Give the position of every malaria parasite and every leukocyte.
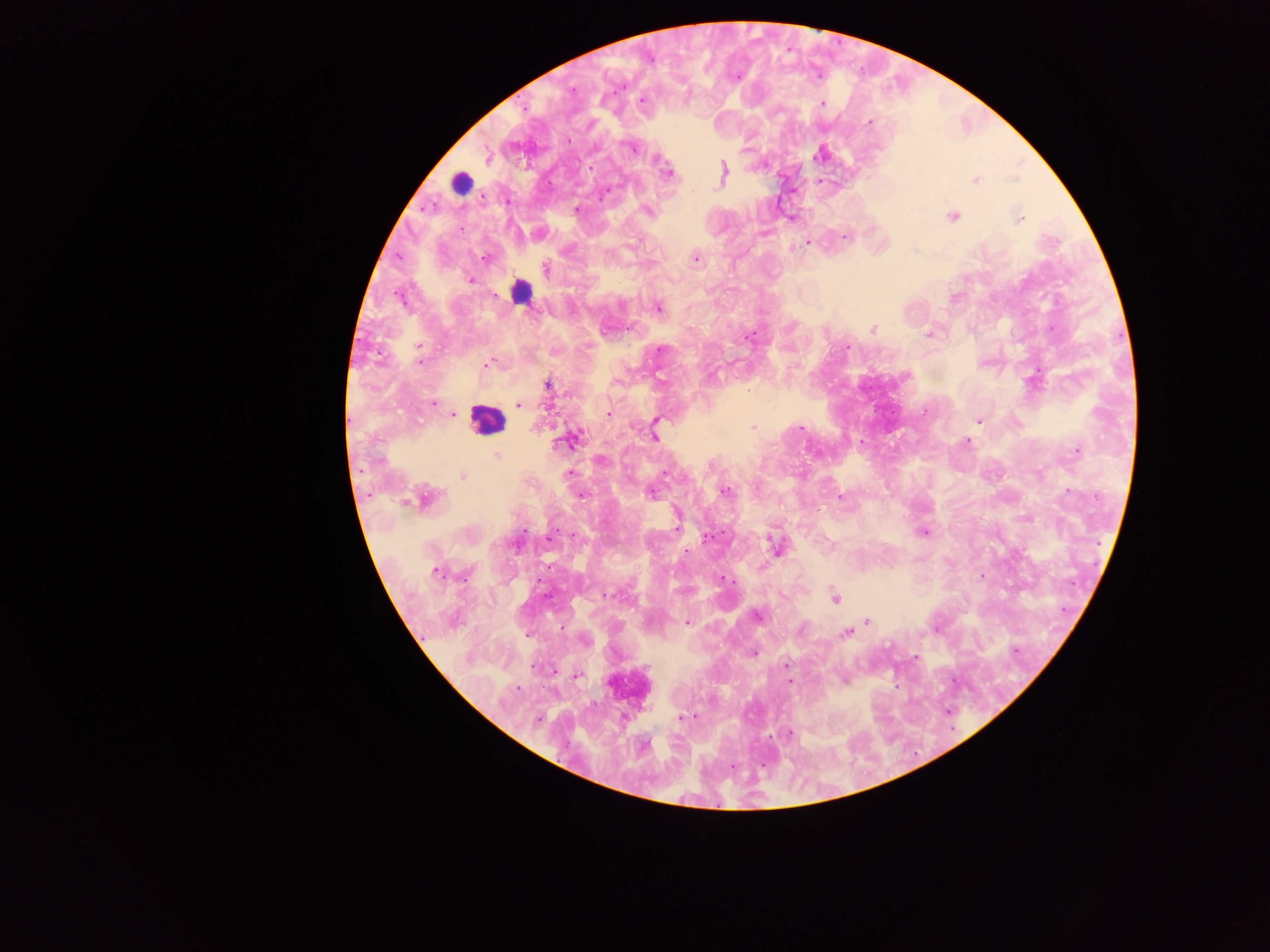

Approximate centers as (x, y) in pixels.
Malaria parasites: (642, 99), (823, 104), (869, 122), (569, 141), (631, 148), (487, 157), (658, 160), (590, 168), (723, 169), (669, 174), (975, 180), (604, 193), (507, 202), (577, 209), (648, 211), (952, 215), (791, 218), (1019, 219), (845, 237), (807, 243), (485, 259), (696, 259), (546, 269), (469, 280), (401, 300), (657, 308), (872, 330), (929, 334), (749, 336), (420, 347), (847, 348), (661, 349), (419, 362), (487, 365), (548, 386), (433, 404), (519, 405), (925, 411), (608, 413), (454, 414), (655, 420), (979, 421), (753, 427), (800, 428), (653, 437), (573, 440), (967, 441), (1077, 450), (497, 456), (600, 460), (665, 473), (569, 474), (462, 476), (726, 491), (1068, 491), (653, 494), (580, 495), (840, 498), (426, 499), (677, 526), (924, 532), (574, 535), (707, 537), (549, 539), (775, 545), (686, 552), (436, 572), (982, 576), (606, 595), (835, 597), (758, 617), (867, 620), (686, 623), (801, 630), (847, 634), (754, 653), (915, 658), (785, 664), (578, 674), (518, 689), (681, 717), (538, 719), (789, 733).
Leukocytes: (460, 182), (520, 291), (487, 421).

Summary:
  - Field of view: single
  - Preparation: thick blood smear
  - Capture: mobile-phone photograph through a microscope
  - Image size: 1270×952 pixels
  - Country: Ghana